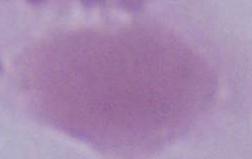
identification = red blood cell
magnification = 1000x
modality = micrograph